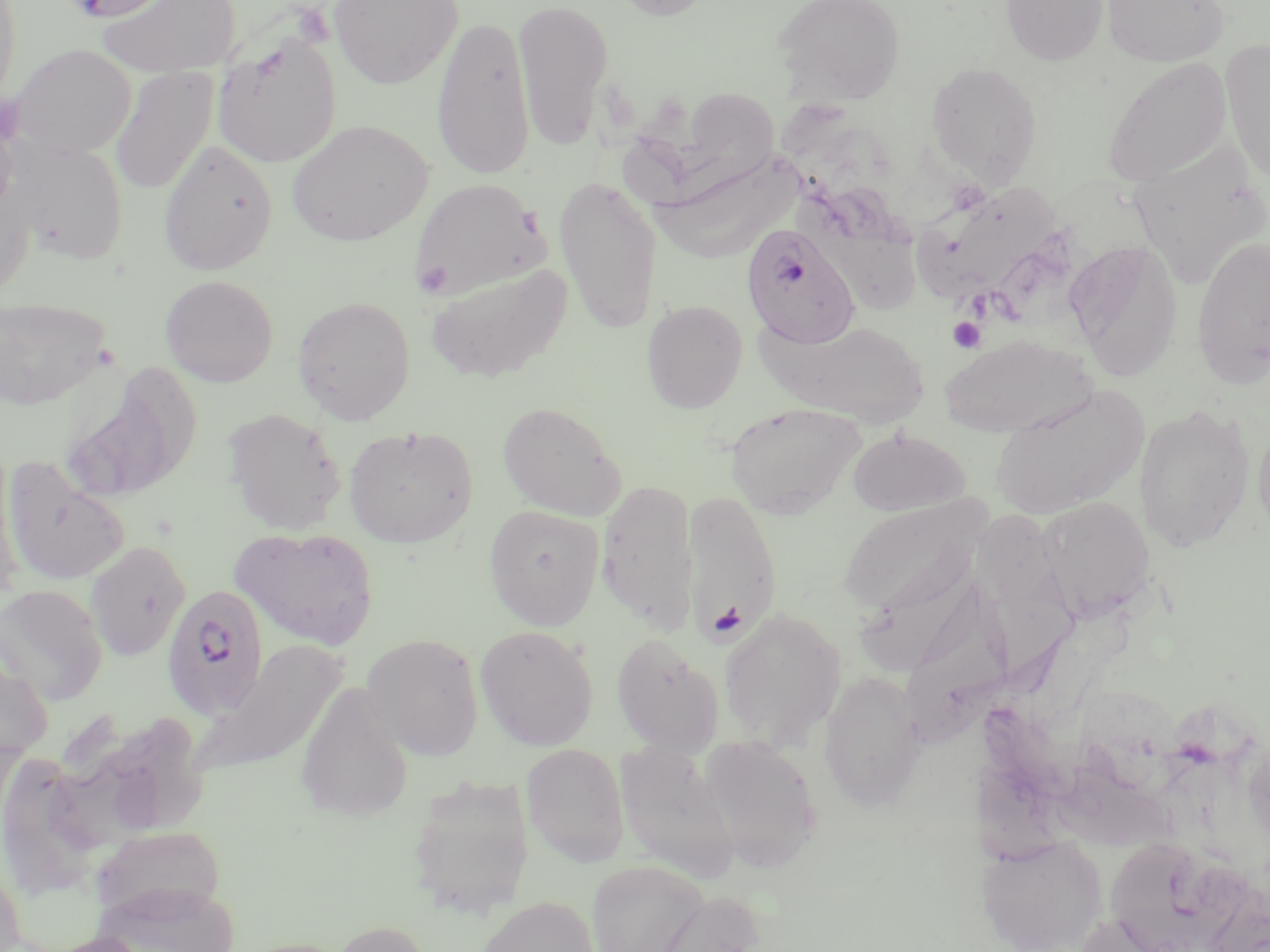

Approximate bounding boxes as [x1, y1, x2, y2] in pixels. Platelet locations: [415, 260, 453, 297], [948, 317, 986, 353], [711, 601, 746, 640]. Plasmodium falciparum-infected red blood cell locations: [741, 222, 860, 350], [161, 582, 269, 719]. Uninfected red blood cell locations: [65, 0, 181, 21], [95, 0, 242, 78], [327, 0, 462, 89], [513, 0, 615, 150], [606, 0, 721, 21], [772, 0, 907, 106], [1001, 0, 1109, 66], [1102, 0, 1229, 66], [0, 1, 22, 111], [432, 14, 536, 181], [211, 33, 341, 167], [1220, 39, 1270, 187], [10, 43, 136, 160], [1102, 56, 1233, 188], [926, 62, 1041, 183], [109, 67, 216, 196], [616, 88, 790, 207], [286, 119, 433, 246], [158, 139, 278, 275], [13, 140, 129, 266], [1127, 142, 1270, 289], [641, 155, 813, 270], [554, 174, 662, 334], [410, 178, 548, 301], [795, 180, 927, 315], [916, 181, 1065, 302], [1191, 235, 1270, 387], [1066, 240, 1183, 380], [424, 262, 572, 383], [160, 274, 278, 387], [0, 295, 112, 410], [292, 296, 416, 424], [641, 299, 747, 414], [776, 319, 928, 426], [940, 334, 1095, 437], [62, 374, 191, 503], [987, 384, 1149, 522], [497, 401, 627, 520], [724, 403, 865, 520], [1133, 403, 1255, 553], [221, 406, 347, 535], [1253, 418, 1270, 543], [343, 424, 478, 549], [847, 427, 970, 517], [0, 447, 23, 599], [2, 455, 131, 586], [596, 481, 698, 633], [683, 492, 781, 646], [973, 494, 1087, 679], [837, 496, 989, 620], [1036, 496, 1155, 622], [484, 504, 604, 630], [231, 526, 380, 650], [85, 541, 191, 661], [858, 547, 994, 683], [0, 584, 108, 706], [907, 585, 1019, 759], [719, 607, 846, 750], [475, 624, 599, 751], [610, 632, 726, 756], [361, 633, 484, 760], [190, 640, 347, 786], [0, 651, 53, 767], [818, 670, 926, 811], [295, 682, 414, 823], [115, 719, 209, 827], [696, 734, 822, 871], [521, 742, 630, 867], [614, 742, 739, 882], [47, 743, 158, 863], [5, 747, 105, 899], [1057, 760, 1187, 856], [406, 777, 534, 920], [88, 826, 228, 925], [976, 834, 1107, 952], [1111, 843, 1251, 952], [0, 852, 26, 952], [586, 859, 708, 952], [93, 882, 243, 952], [644, 889, 765, 952], [474, 895, 600, 952], [1071, 914, 1178, 952], [329, 920, 434, 952], [42, 931, 155, 952]. Slide-level diagnosis: Plasmodium falciparum. Thin blood smear. Image is 1270×952 pixels. Single field of view. Light microscopy. 1000x magnification. May-Grünwald-Giemsa-stained preparation.